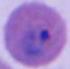

Micrograph. A Plasmodium parasite is shown. 400x or 1000x magnification.